Outline each blood parasite and name the species.
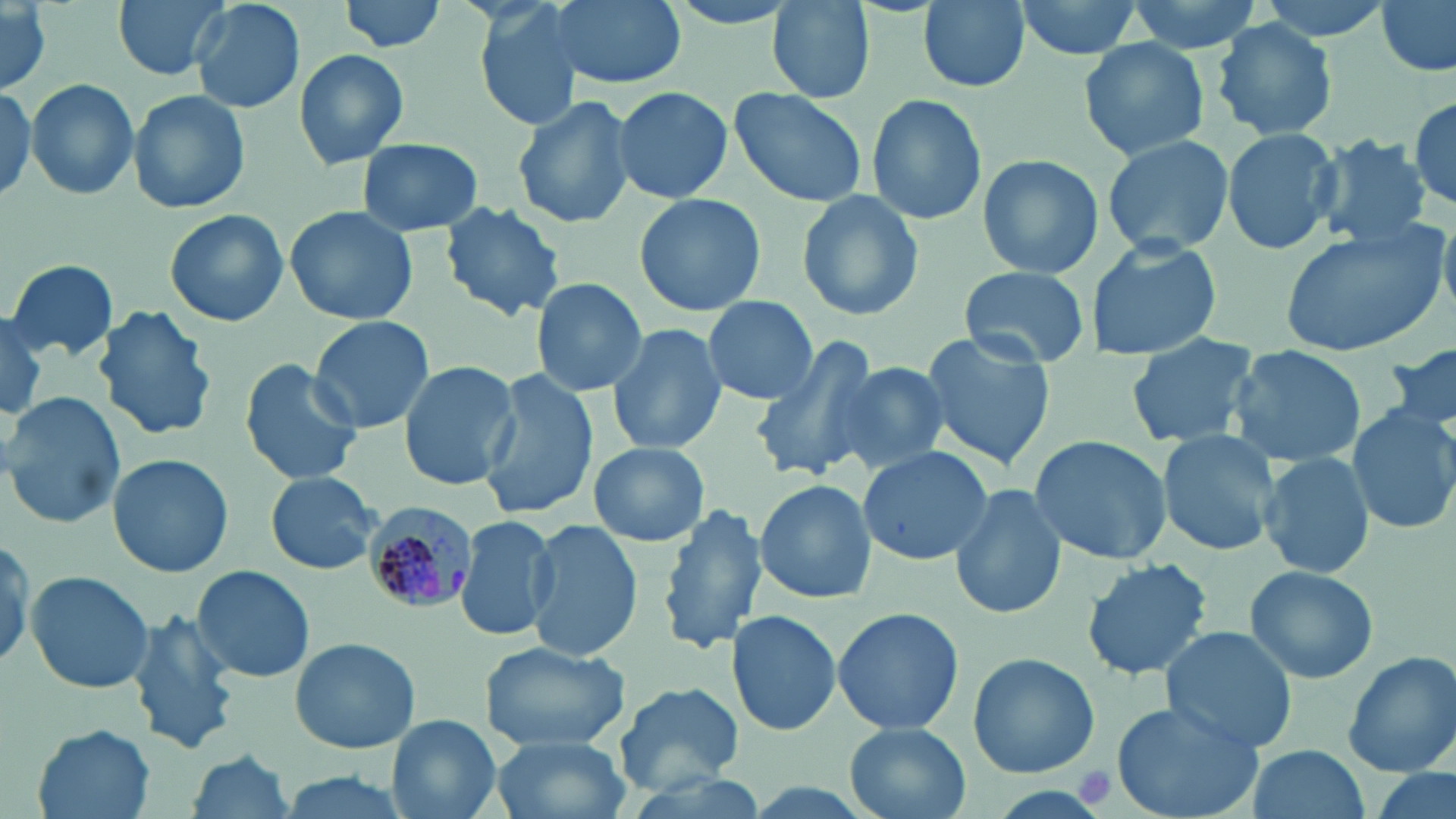

Approximate bounding boxes as named x1/y1/x2/y2 corners in pixels.
Plasmodium malariae-infected red blood cells: (x1=361, y1=499, x2=480, y2=615).
No Plasmodium falciparum, Plasmodium ovale, Plasmodium vivax, Babesia divergens, or Trypanosoma brucei observed.

Uninfected red blood cell locations: (x1=113, y1=0, x2=231, y2=81), (x1=190, y1=0, x2=304, y2=114), (x1=339, y1=0, x2=449, y2=55), (x1=470, y1=0, x2=589, y2=130), (x1=546, y1=0, x2=684, y2=90), (x1=657, y1=0, x2=814, y2=31), (x1=916, y1=0, x2=1032, y2=93), (x1=1011, y1=0, x2=1146, y2=61), (x1=1120, y1=0, x2=1267, y2=57), (x1=1374, y1=0, x2=1454, y2=76), (x1=770, y1=1, x2=875, y2=102), (x1=0, y1=4, x2=55, y2=95), (x1=1209, y1=19, x2=1338, y2=140), (x1=1079, y1=37, x2=1210, y2=162), (x1=294, y1=48, x2=410, y2=169), (x1=26, y1=78, x2=139, y2=201), (x1=0, y1=84, x2=36, y2=202), (x1=612, y1=85, x2=734, y2=205), (x1=730, y1=89, x2=868, y2=208), (x1=128, y1=90, x2=251, y2=214), (x1=1409, y1=94, x2=1455, y2=212), (x1=512, y1=95, x2=634, y2=232), (x1=866, y1=96, x2=986, y2=226), (x1=1222, y1=127, x2=1341, y2=255), (x1=1100, y1=133, x2=1234, y2=255), (x1=1312, y1=134, x2=1430, y2=250), (x1=358, y1=137, x2=483, y2=237), (x1=979, y1=151, x2=1104, y2=279), (x1=795, y1=189, x2=925, y2=322), (x1=632, y1=193, x2=767, y2=318), (x1=438, y1=201, x2=568, y2=322), (x1=284, y1=205, x2=419, y2=325), (x1=163, y1=207, x2=290, y2=328), (x1=1278, y1=225, x2=1449, y2=357), (x1=1087, y1=236, x2=1224, y2=359), (x1=4, y1=259, x2=118, y2=365), (x1=957, y1=266, x2=1094, y2=370), (x1=530, y1=278, x2=648, y2=396), (x1=701, y1=294, x2=817, y2=405), (x1=96, y1=305, x2=217, y2=439), (x1=0, y1=313, x2=52, y2=423), (x1=307, y1=314, x2=436, y2=432), (x1=607, y1=323, x2=728, y2=456), (x1=1124, y1=330, x2=1261, y2=448), (x1=918, y1=332, x2=1056, y2=469), (x1=749, y1=334, x2=881, y2=482), (x1=1385, y1=343, x2=1455, y2=441), (x1=1226, y1=344, x2=1365, y2=466), (x1=239, y1=358, x2=365, y2=486), (x1=398, y1=360, x2=519, y2=489), (x1=829, y1=363, x2=949, y2=477), (x1=477, y1=370, x2=596, y2=521), (x1=2, y1=389, x2=125, y2=529), (x1=1349, y1=402, x2=1456, y2=537), (x1=1157, y1=432, x2=1282, y2=557), (x1=1028, y1=435, x2=1173, y2=565), (x1=588, y1=441, x2=711, y2=548), (x1=858, y1=446, x2=992, y2=567), (x1=1260, y1=453, x2=1375, y2=580), (x1=108, y1=454, x2=234, y2=577), (x1=266, y1=471, x2=382, y2=575), (x1=753, y1=479, x2=877, y2=606), (x1=949, y1=483, x2=1066, y2=619), (x1=658, y1=502, x2=765, y2=654), (x1=456, y1=511, x2=558, y2=644), (x1=524, y1=517, x2=645, y2=664), (x1=1080, y1=559, x2=1213, y2=681), (x1=190, y1=564, x2=315, y2=683), (x1=1245, y1=565, x2=1379, y2=683), (x1=25, y1=569, x2=154, y2=694), (x1=831, y1=606, x2=964, y2=736), (x1=127, y1=609, x2=242, y2=757), (x1=729, y1=609, x2=845, y2=736), (x1=1159, y1=625, x2=1303, y2=755), (x1=290, y1=637, x2=421, y2=754), (x1=478, y1=639, x2=632, y2=751), (x1=1342, y1=650, x2=1456, y2=776), (x1=967, y1=652, x2=1099, y2=778), (x1=615, y1=681, x2=744, y2=792), (x1=1112, y1=700, x2=1265, y2=819), (x1=386, y1=714, x2=501, y2=819), (x1=844, y1=723, x2=970, y2=819), (x1=32, y1=725, x2=155, y2=818), (x1=490, y1=733, x2=633, y2=819), (x1=1243, y1=744, x2=1371, y2=819), (x1=185, y1=751, x2=297, y2=819), (x1=1368, y1=764, x2=1454, y2=819), (x1=269, y1=772, x2=420, y2=819). Platelet locations: (x1=1072, y1=763, x2=1117, y2=808). Slide-level diagnosis: Plasmodium malariae. Optical microscopy. Captured at 1000x magnification. May-Grünwald-Giemsa stain. Single field of view. Image is 1456×819 pixels. Thin blood smear.